Name the parasite shown.
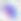
This is Toxoplasma gondii.

Summary:
  - Modality: photomicrograph
  - Magnification: 400x